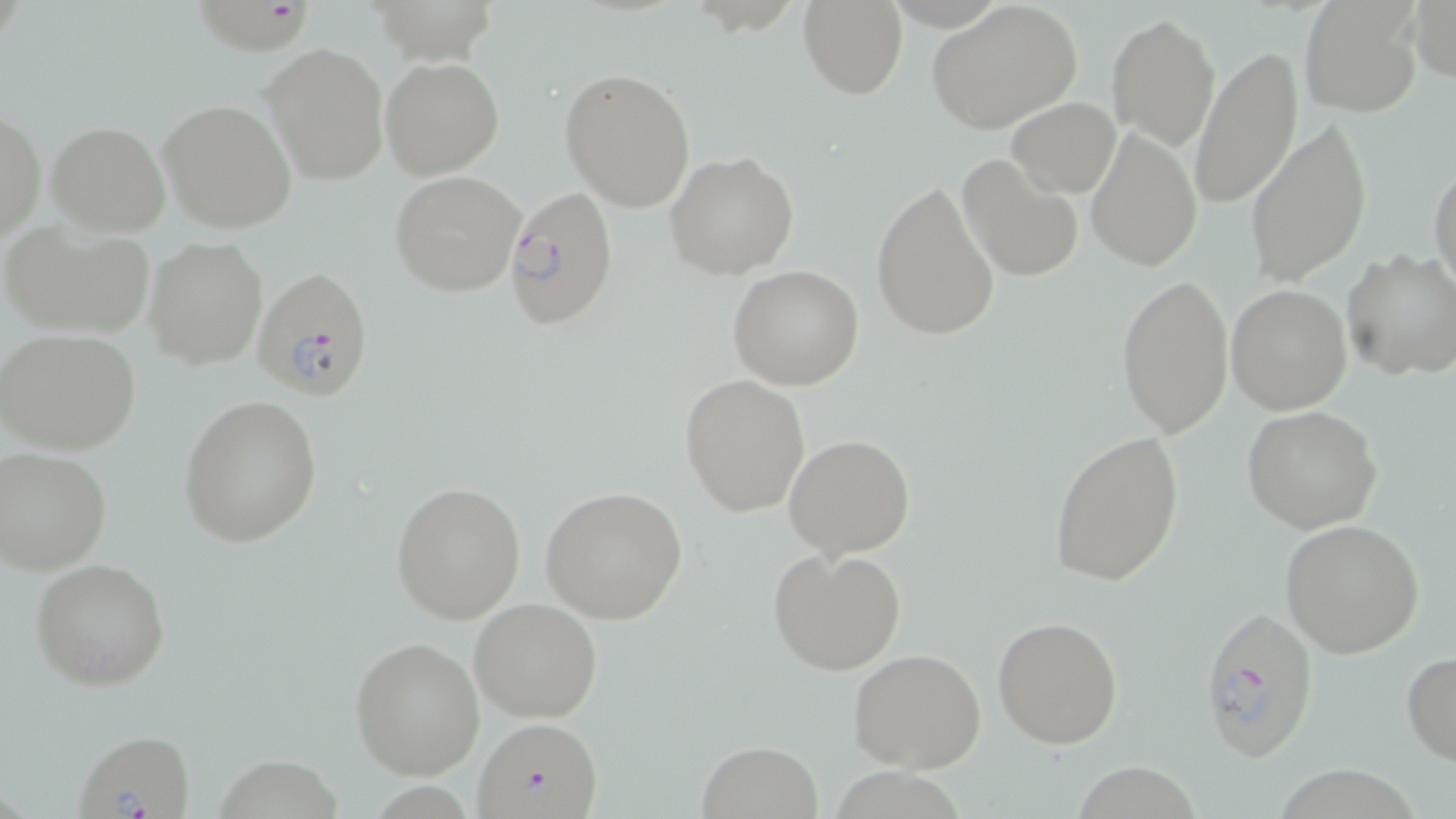 Approximate bounding boxes as (x1,y1)-(x2,y2) corner pairs in pixels. Uninfected red blood cell locations: (1409,0)-(1455,85), (797,1)-(908,98), (925,1)-(1083,134), (1299,3)-(1421,118), (1106,15)-(1221,148), (262,42)-(388,184), (1191,47)-(1303,209), (379,56)-(505,179), (559,68)-(697,212), (1007,97)-(1121,198), (158,98)-(297,233), (0,109)-(45,244), (1244,117)-(1369,288), (46,120)-(170,236), (1086,125)-(1201,273), (665,151)-(799,281), (957,152)-(1084,285), (1430,165)-(1455,296), (390,171)-(525,296), (870,179)-(1001,342), (2,218)-(155,340), (145,237)-(268,369), (1341,249)-(1456,381), (728,266)-(865,390), (1116,275)-(1233,438), (1226,284)-(1351,413), (0,327)-(141,455), (680,375)-(809,516), (179,396)-(323,547), (1242,407)-(1385,536), (1047,431)-(1186,587), (784,433)-(915,558), (1,447)-(115,576), (392,480)-(526,624), (539,486)-(688,625), (1279,518)-(1426,659), (767,545)-(907,675), (29,557)-(171,691), (469,597)-(603,722), (992,616)-(1124,749), (349,636)-(485,780), (848,647)-(987,774), (1401,651)-(1456,765), (695,740)-(823,818), (217,755)-(346,819), (1072,757)-(1211,819), (833,763)-(973,819), (1278,767)-(1424,819), (377,783)-(468,819). Plasmodium falciparum-infected red blood cell locations: (197,0)-(323,59), (502,186)-(619,329), (253,268)-(378,402), (1199,606)-(1320,763), (474,714)-(605,819), (73,729)-(197,819). Slide-level diagnosis: Plasmodium falciparum. Optical microscopy. Image is 1456×819 pixels. One field of a larger specimen. May-Grünwald-Giemsa stain. 1000x magnification. Thin blood film.